Report the malaria status of this cell.
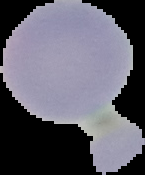

It is uninfected.

Summary:
  - Image type: segmented cell region with the area outside set to black
  - Image size: 145×175 pixels
  - Preparation: thin blood film